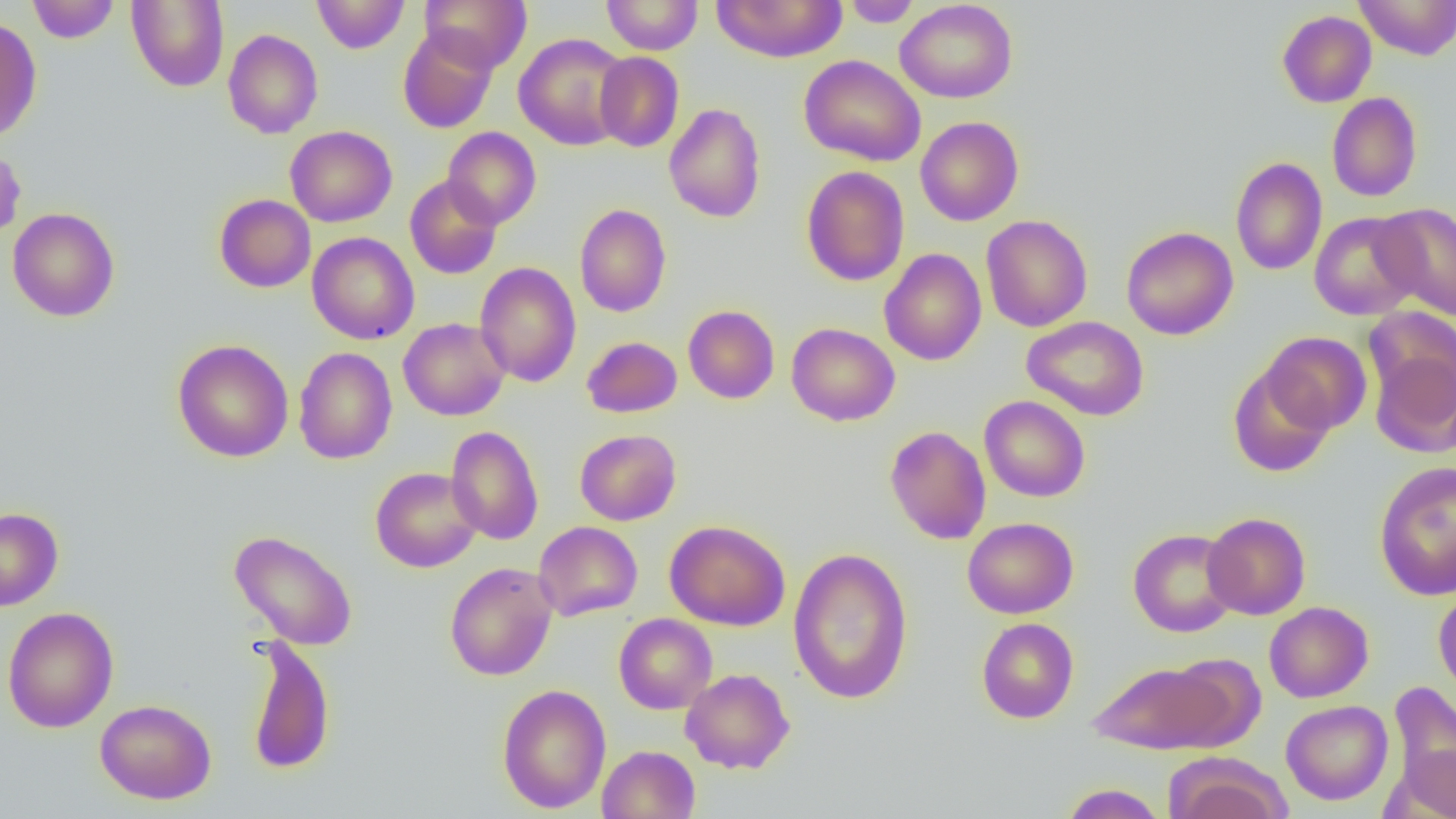
Summary:
  - Coordinate format: approximate bounding boxes as named x1/y1/x2/y2 corners in pixels
  - Uninfected red blood cell locations: (x1=27, y1=0, x2=120, y2=43), (x1=126, y1=0, x2=229, y2=91), (x1=312, y1=0, x2=409, y2=54), (x1=421, y1=0, x2=531, y2=72), (x1=601, y1=0, x2=703, y2=55), (x1=712, y1=0, x2=848, y2=63), (x1=895, y1=0, x2=1018, y2=103), (x1=1355, y1=0, x2=1456, y2=59), (x1=841, y1=1, x2=923, y2=27), (x1=1277, y1=10, x2=1376, y2=108), (x1=0, y1=16, x2=42, y2=142), (x1=397, y1=27, x2=498, y2=133), (x1=222, y1=29, x2=323, y2=138), (x1=513, y1=32, x2=632, y2=150), (x1=594, y1=51, x2=684, y2=152), (x1=798, y1=54, x2=926, y2=167), (x1=1326, y1=92, x2=1423, y2=202), (x1=664, y1=103, x2=766, y2=223), (x1=915, y1=116, x2=1024, y2=226), (x1=285, y1=125, x2=397, y2=227), (x1=442, y1=127, x2=542, y2=229), (x1=0, y1=143, x2=26, y2=243), (x1=1230, y1=157, x2=1327, y2=275), (x1=801, y1=166, x2=910, y2=286), (x1=404, y1=175, x2=502, y2=280), (x1=214, y1=194, x2=316, y2=292), (x1=574, y1=203, x2=672, y2=317), (x1=1373, y1=203, x2=1456, y2=320), (x1=7, y1=207, x2=120, y2=321), (x1=1309, y1=211, x2=1422, y2=320), (x1=980, y1=214, x2=1093, y2=332), (x1=1121, y1=226, x2=1238, y2=340), (x1=307, y1=232, x2=419, y2=345), (x1=879, y1=248, x2=987, y2=366), (x1=475, y1=262, x2=581, y2=387), (x1=682, y1=305, x2=780, y2=404), (x1=1363, y1=306, x2=1456, y2=408), (x1=1022, y1=316, x2=1150, y2=421), (x1=398, y1=317, x2=509, y2=421), (x1=786, y1=322, x2=900, y2=426), (x1=1261, y1=331, x2=1372, y2=435), (x1=581, y1=336, x2=682, y2=418), (x1=172, y1=339, x2=294, y2=463), (x1=293, y1=347, x2=397, y2=464), (x1=1369, y1=348, x2=1456, y2=458), (x1=1227, y1=364, x2=1336, y2=478), (x1=979, y1=395, x2=1090, y2=502), (x1=445, y1=425, x2=544, y2=545), (x1=884, y1=426, x2=991, y2=544), (x1=575, y1=429, x2=681, y2=525), (x1=1374, y1=461, x2=1456, y2=600), (x1=370, y1=466, x2=482, y2=573), (x1=0, y1=507, x2=64, y2=610), (x1=1202, y1=512, x2=1311, y2=620), (x1=962, y1=517, x2=1078, y2=619), (x1=664, y1=519, x2=791, y2=631), (x1=533, y1=521, x2=642, y2=621), (x1=1127, y1=528, x2=1241, y2=638), (x1=229, y1=529, x2=358, y2=650), (x1=787, y1=546, x2=914, y2=704), (x1=444, y1=561, x2=558, y2=681), (x1=1433, y1=587, x2=1456, y2=702), (x1=1264, y1=601, x2=1374, y2=702), (x1=2, y1=606, x2=119, y2=733), (x1=614, y1=613, x2=717, y2=714), (x1=976, y1=617, x2=1079, y2=724), (x1=244, y1=635, x2=336, y2=775), (x1=1087, y1=658, x2=1242, y2=755), (x1=680, y1=668, x2=795, y2=774), (x1=1387, y1=681, x2=1456, y2=803), (x1=497, y1=684, x2=612, y2=813), (x1=95, y1=699, x2=217, y2=804), (x1=1281, y1=700, x2=1393, y2=805), (x1=1391, y1=742, x2=1456, y2=819), (x1=597, y1=744, x2=700, y2=819), (x1=1165, y1=754, x2=1290, y2=819), (x1=1060, y1=783, x2=1167, y2=819)
  - Slide-level diagnosis: negative for blood parasites
  - Image size: 1456×819 pixels
  - Preparation: thin blood film
  - Magnification: 1000x
  - Field of view: single
  - Modality: optical microscopy